Mark where platelets are.
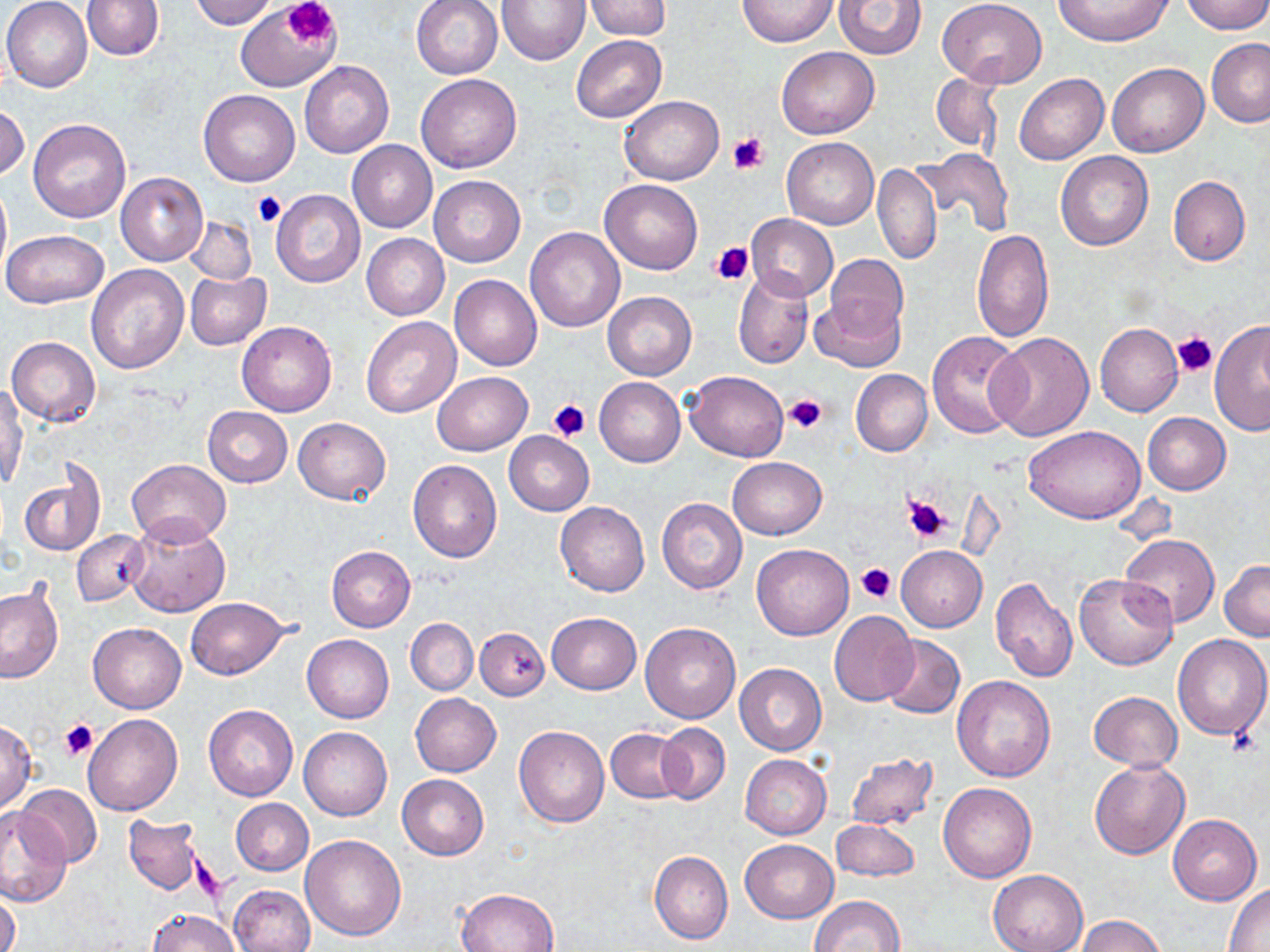
Approximate bounding boxes as [x1, y1, x2, y2] in pixels.
Platelets: [286, 0, 338, 45], [728, 132, 770, 176], [254, 191, 286, 227], [710, 239, 754, 284], [1173, 331, 1217, 377], [784, 393, 826, 433], [548, 399, 590, 441], [900, 491, 955, 545], [855, 563, 897, 603], [60, 719, 98, 761].

Summary:
  - Uninfected red blood cell locations: [1, 0, 93, 93], [81, 0, 163, 59], [188, 0, 277, 29], [411, 0, 503, 79], [585, 0, 672, 39], [737, 0, 836, 47], [834, 0, 926, 58], [1053, 0, 1171, 46], [1180, 0, 1270, 34], [939, 1, 1048, 87], [498, 2, 589, 66], [236, 7, 338, 92], [571, 35, 667, 122], [1206, 38, 1270, 127], [777, 46, 879, 139], [300, 60, 393, 158], [1107, 62, 1209, 157], [930, 72, 1002, 153], [416, 73, 522, 173], [1014, 73, 1108, 164], [198, 89, 299, 187], [620, 95, 723, 184], [0, 103, 29, 180], [28, 118, 131, 224], [781, 137, 878, 229], [347, 140, 436, 232], [913, 148, 1014, 235], [1055, 150, 1154, 251], [873, 164, 941, 264], [116, 172, 208, 265], [428, 175, 524, 266], [1168, 175, 1250, 265], [0, 178, 11, 281], [601, 178, 703, 274], [271, 190, 365, 288], [746, 213, 838, 301], [183, 214, 258, 284], [525, 226, 626, 332], [2, 229, 109, 308], [970, 229, 1053, 342], [362, 234, 449, 320], [825, 253, 908, 336], [85, 265, 189, 375], [733, 268, 813, 369], [185, 271, 271, 350], [450, 273, 542, 371], [603, 291, 696, 380], [809, 293, 905, 372], [361, 317, 461, 417], [1209, 320, 1270, 438], [237, 321, 336, 417], [1095, 322, 1183, 417], [926, 331, 1025, 439], [987, 331, 1096, 441], [6, 336, 99, 425], [684, 370, 788, 462], [851, 370, 932, 456], [433, 372, 532, 455], [594, 376, 685, 467], [1, 383, 27, 488], [203, 407, 292, 486], [1143, 413, 1231, 494], [294, 417, 391, 503], [1024, 425, 1146, 524], [504, 431, 595, 515], [728, 456, 827, 540], [127, 458, 231, 547], [407, 460, 502, 563], [20, 472, 102, 555], [656, 496, 748, 594], [555, 502, 649, 597], [124, 514, 232, 617], [73, 530, 149, 607], [1120, 534, 1219, 628], [751, 544, 853, 639], [326, 545, 415, 632], [896, 545, 986, 631], [1220, 560, 1270, 640], [1074, 572, 1177, 671], [990, 577, 1080, 682], [0, 584, 63, 685], [186, 596, 288, 679], [829, 610, 920, 706], [547, 613, 641, 693], [406, 618, 478, 695], [640, 621, 741, 723], [89, 623, 186, 714], [475, 626, 549, 699], [1171, 634, 1270, 740], [301, 635, 393, 723], [879, 635, 966, 719], [735, 663, 826, 755], [951, 675, 1056, 781], [1088, 691, 1183, 771], [411, 693, 501, 777], [203, 704, 298, 801], [84, 714, 182, 817], [0, 721, 36, 811], [655, 723, 730, 804], [513, 725, 609, 827], [299, 727, 392, 821], [606, 727, 689, 803], [844, 752, 940, 832], [740, 754, 832, 840], [1088, 760, 1190, 859], [396, 775, 488, 860], [938, 782, 1037, 882], [15, 784, 103, 869], [232, 799, 314, 876], [0, 806, 71, 908], [1168, 814, 1261, 905], [123, 816, 206, 896], [831, 820, 921, 882], [300, 835, 407, 940], [739, 839, 838, 923], [649, 850, 733, 945], [988, 868, 1089, 952], [1225, 882, 1270, 950], [231, 884, 315, 952], [1, 889, 20, 952], [455, 889, 561, 951], [808, 895, 904, 952], [147, 909, 238, 952], [1075, 915, 1167, 952]
  - Slide-level diagnosis: negative for blood parasites
  - Preparation: thin blood smear
  - Stain: May-Grünwald-Giemsa
  - Magnification: 1000x
  - Modality: optical microscopy
  - Field of view: single
  - Image size: 1270×952 pixels